Classify this cell by malaria status.
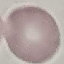

It is uninfected.

Thin smear of blood. Acquired by smartphone through the microscope eyepiece. Cell patch, automatically extracted from a larger field of view and resized to 64 × 64 pixels. Giemsa stain.